Assess for malaria.
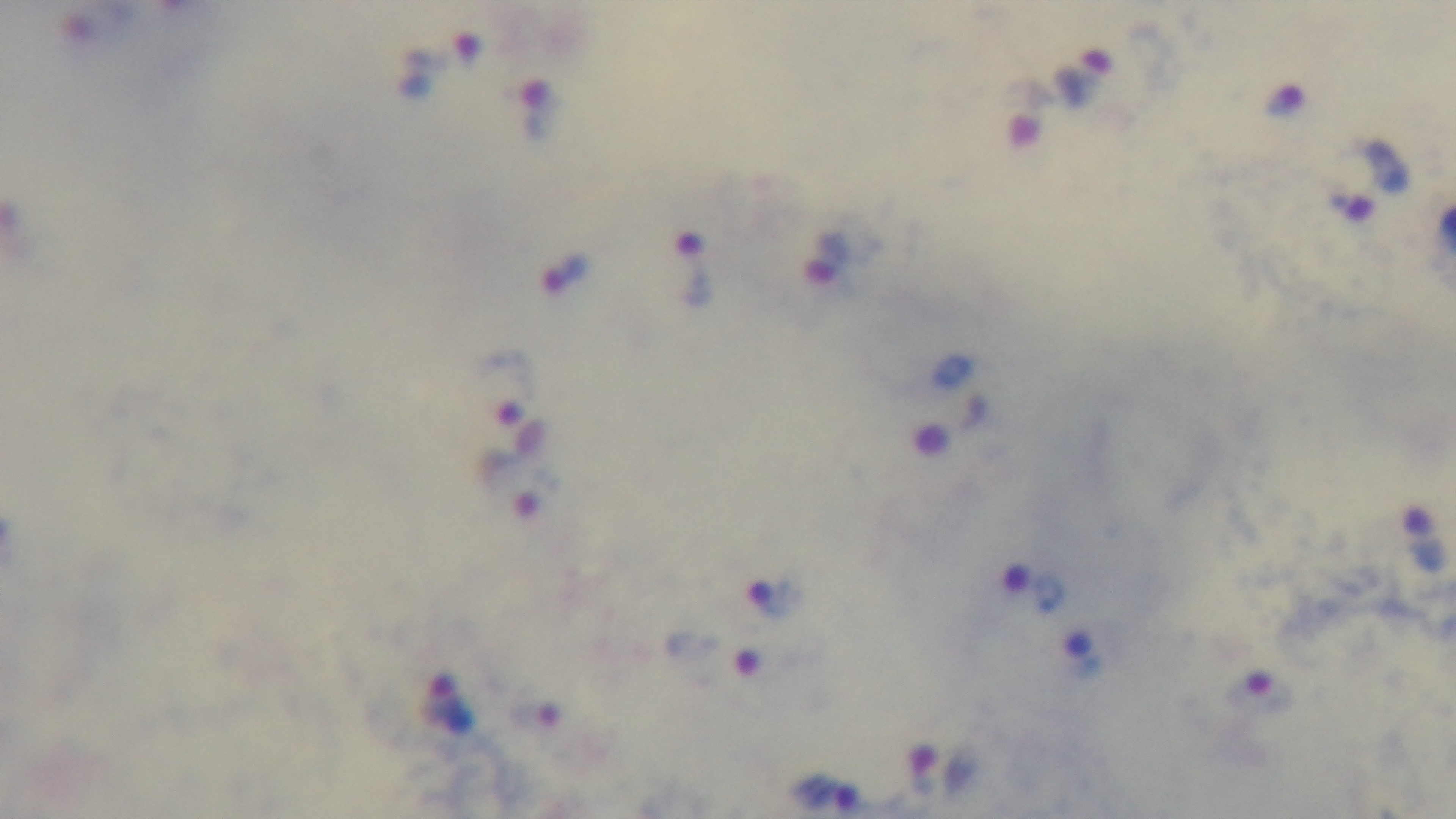

Infected.

Summary:
  - Field of view: single
  - Modality: light microscopy
  - Preparation: thick smear
  - Capture: mounted 4K digital camera
  - Objective: 100x oil immersion
  - Stain: Giemsa